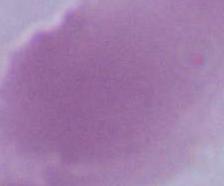

magnification: 1000x
identification: red blood cell
modality: micrograph